Locate platelets.
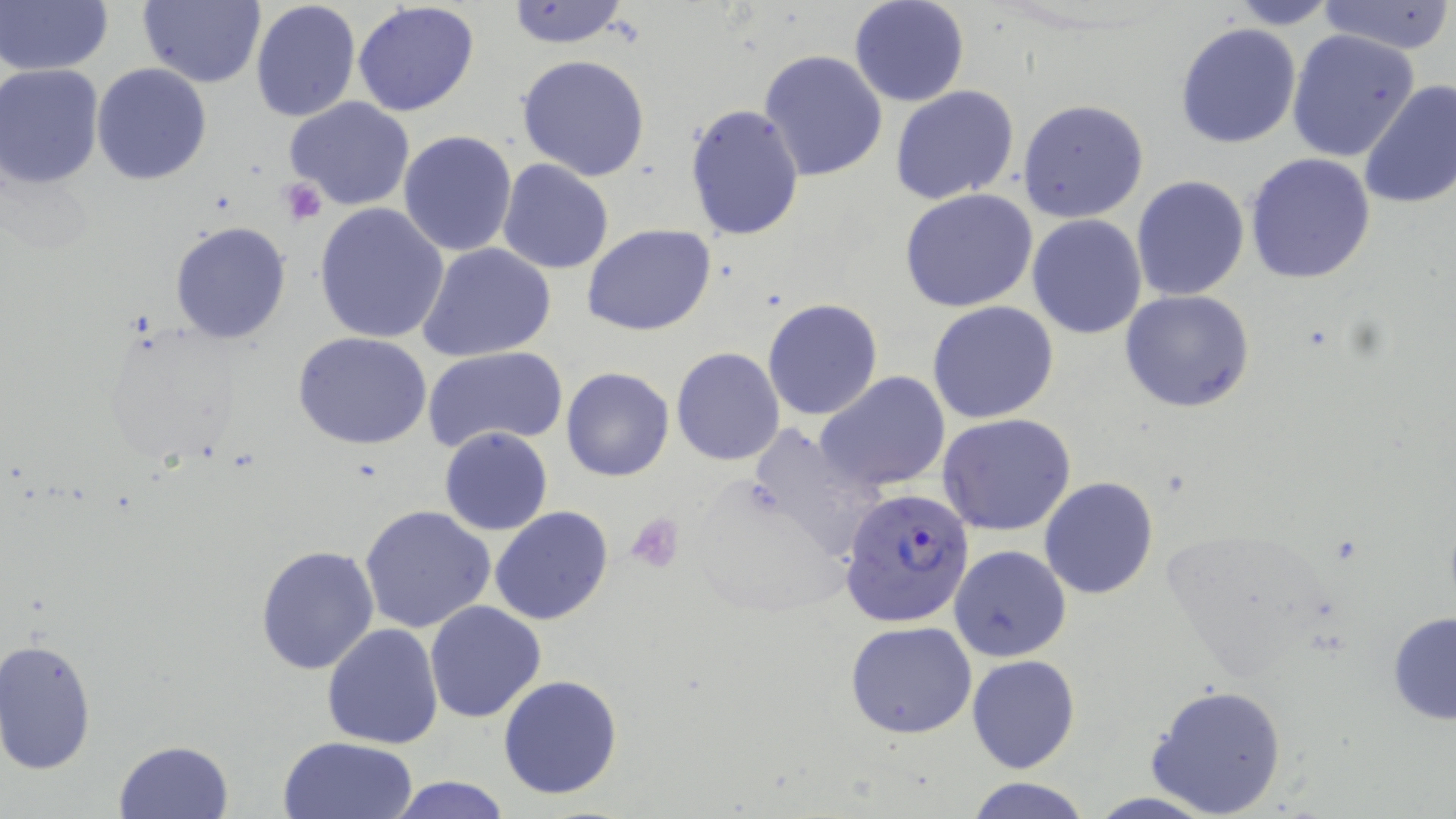

Approximate bounding boxes as (x1,y1)-(x2,y2) corner pairs in pixels.
Platelets: (278,178)-(328,225), (626,513)-(684,574).

slide_level_diagnosis: Plasmodium falciparum
uninfected_red_blood_cell_locations: 'approximate bounding boxes as (x1,y1)-(x2,y2) corner pairs in pixels: (135,0)-(266,88), (250,0)-(361,121), (848,0)-(970,108), (1315,0)-(1456,54), (1,1)-(112,77), (352,1)-(481,118), (504,1)-(632,50), (1223,1)-(1343,29), (1175,22)-(1303,149), (1286,29)-(1419,162), (758,49)-(888,181), (516,53)-(650,181), (92,62)-(212,185), (0,64)-(105,187), (1359,79)-(1456,210), (890,84)-(1021,205), (284,96)-(416,211), (1018,99)-(1149,223), (684,104)-(806,242), (399,130)-(517,256), (1245,153)-(1377,285), (497,158)-(614,274), (1132,176)-(1248,301), (898,189)-(1041,313), (314,201)-(449,343), (1026,215)-(1149,340), (169,220)-(292,344), (582,224)-(717,335), (417,242)-(557,363), (1120,290)-(1255,413), (762,299)-(884,421), (926,300)-(1059,424), (98,321)-(248,464), (291,330)-(433,450), (670,346)-(785,466), (424,347)-(566,453), (561,367)-(673,481), (816,372)-(951,494), (938,414)-(1078,536), (746,423)-(887,561), (439,427)-(551,536), (1040,477)-(1158,600), (359,504)-(496,633), (490,506)-(615,626), (949,544)-(1072,665), (256,545)-(381,675), (424,599)-(546,722), (1386,611)-(1456,725), (844,620)-(977,739), (322,624)-(446,749), (0,637)-(98,774), (967,653)-(1080,774), (497,674)-(623,799), (1145,684)-(1289,817), (277,735)-(418,818), (115,740)-(234,817), (385,775)-(515,818), (965,777)-(1093,819)'
stain: May-Grünwald-Giemsa
image_size: 1456×819 pixels
modality: optical microscopy
plasmodium_falciparum_infected_red_blood_cell_locations: 'approximate bounding boxes as (x1,y1)-(x2,y2) corner pairs in pixels: (839,485)-(975,630)'
field_of_view: one of a larger specimen
preparation: thin blood smear
magnification: 1000x